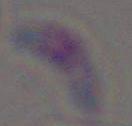

Toxoplasma gondii is seen. Micrograph. 1000x magnification.